State the blood parasite species.
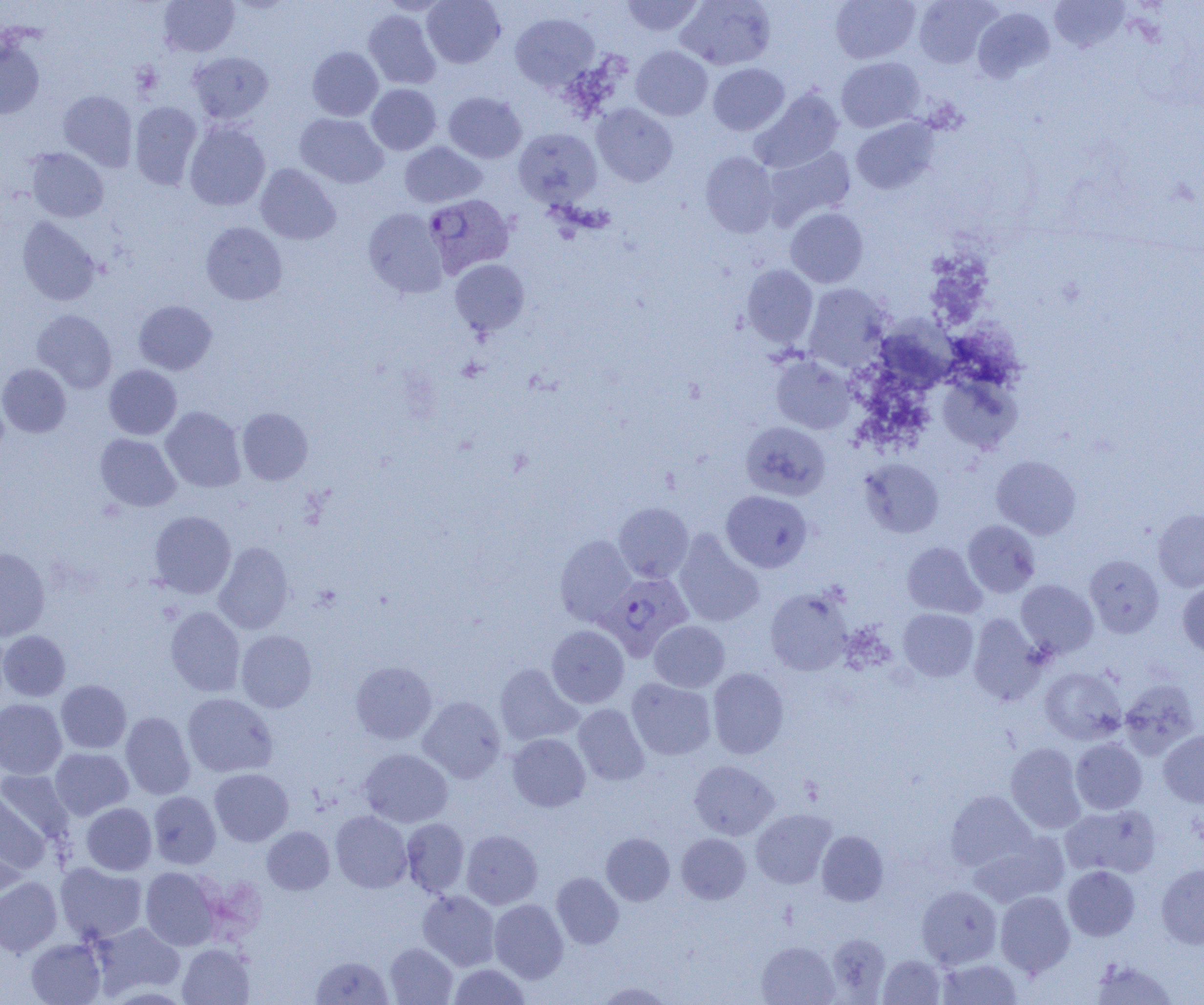
Plasmodium vivax.

uninfected_red_blood_cell_locations: 'approximate bounding boxes as (x1, y1, x2, y2) in pixels: (159, 0, 240, 57), (379, 0, 451, 16), (422, 0, 505, 68), (620, 0, 705, 37), (676, 0, 775, 70), (830, 0, 920, 63), (913, 0, 1001, 68), (1048, 0, 1130, 53), (972, 7, 1055, 83), (363, 10, 441, 89), (510, 12, 599, 92), (0, 37, 45, 119), (307, 46, 383, 121), (631, 46, 712, 121), (188, 51, 273, 125), (836, 57, 925, 132), (708, 63, 789, 135), (367, 84, 441, 155), (750, 88, 844, 173), (58, 90, 138, 171), (443, 92, 526, 163), (130, 102, 202, 190), (592, 103, 678, 186), (295, 113, 388, 188), (851, 118, 939, 195), (184, 121, 270, 211), (514, 128, 602, 208), (400, 142, 486, 208), (763, 146, 856, 229), (26, 147, 108, 222), (700, 152, 779, 237), (256, 164, 340, 244), (364, 208, 448, 298), (785, 208, 868, 288), (17, 217, 101, 306), (201, 222, 288, 305), (450, 259, 530, 336), (742, 265, 818, 348), (803, 284, 892, 373), (133, 300, 217, 375), (32, 309, 117, 393), (881, 316, 968, 390), (771, 356, 855, 434), (0, 363, 71, 438), (104, 365, 182, 440), (937, 374, 1021, 453), (161, 406, 246, 493), (237, 407, 313, 485), (741, 421, 830, 500), (95, 433, 181, 511), (991, 455, 1081, 539), (859, 458, 944, 538), (721, 490, 812, 572), (613, 502, 694, 582), (1153, 508, 1204, 592), (149, 511, 236, 598), (963, 520, 1040, 597), (673, 531, 764, 627), (555, 535, 637, 626), (214, 542, 294, 634), (902, 542, 985, 618), (0, 547, 50, 640), (1085, 554, 1164, 638), (1016, 580, 1098, 658), (1177, 581, 1204, 657), (766, 588, 852, 675), (165, 607, 245, 697), (898, 608, 978, 681), (968, 614, 1047, 705), (649, 621, 730, 692), (547, 625, 629, 708), (0, 630, 70, 701), (236, 630, 317, 712), (351, 660, 437, 744), (494, 663, 583, 746), (1040, 666, 1126, 745), (707, 668, 789, 759), (626, 677, 716, 760), (1119, 678, 1200, 759), (56, 680, 131, 753), (182, 693, 277, 777), (418, 696, 506, 782), (0, 698, 66, 779), (573, 703, 650, 785), (121, 711, 196, 800), (1159, 730, 1204, 807), (507, 733, 590, 811), (1070, 738, 1147, 814), (1005, 742, 1085, 833), (50, 748, 134, 820), (359, 748, 453, 827), (689, 759, 778, 840), (209, 768, 293, 846), (0, 769, 75, 845), (0, 791, 50, 882), (148, 791, 221, 868), (945, 791, 1037, 872), (81, 802, 156, 875), (1060, 804, 1161, 878), (751, 809, 836, 889), (330, 810, 413, 893), (401, 818, 469, 896), (262, 826, 335, 895), (461, 829, 543, 909), (816, 830, 888, 906), (970, 832, 1069, 907), (601, 833, 674, 905), (676, 833, 750, 904), (55, 862, 148, 944), (1156, 864, 1204, 949), (1063, 865, 1139, 940), (140, 867, 221, 950), (552, 872, 623, 948), (0, 876, 62, 956), (916, 885, 1002, 969), (417, 890, 500, 971), (995, 891, 1075, 976), (489, 899, 568, 983), (89, 921, 186, 999), (827, 933, 890, 1002), (26, 938, 106, 1005), (756, 941, 840, 1005), (385, 942, 457, 1004), (177, 943, 254, 1005), (878, 955, 945, 1004), (310, 956, 393, 1004), (936, 957, 1023, 1004), (1090, 958, 1178, 1005), (448, 963, 531, 1004), (592, 981, 675, 1004)'
plasmodium_vivax_infected_red_blood_cell_locations: 'approximate bounding boxes as (x1, y1, x2, y2) in pixels: (420, 191, 511, 276), (601, 572, 693, 660)'
modality: optical microscopy
magnification: 1000x
field_of_view: single
image_size: 1204×1005 pixels
preparation: thin blood film